Point out each malaria parasite.
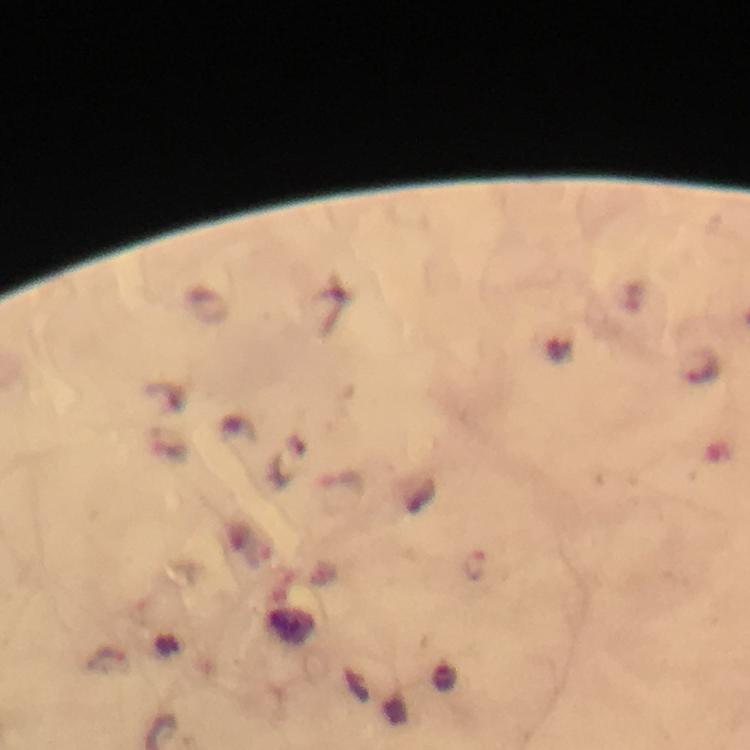
Approximate centers as [x, y] in pixels.
Malaria parasites: [475, 564].

context = from a diagnostic examination for malaria
capture = smartphone mounted on the microscope
immersion oil = applied
cropped from = one field of view
stain = Giemsa
magnification = 100x
preparation = thick blood smear
image size = 750×750 pixels